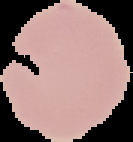
malaria status = uninfected
image type = segmented cell region on a black background
preparation = thin blood film
image size = 133×142 pixels